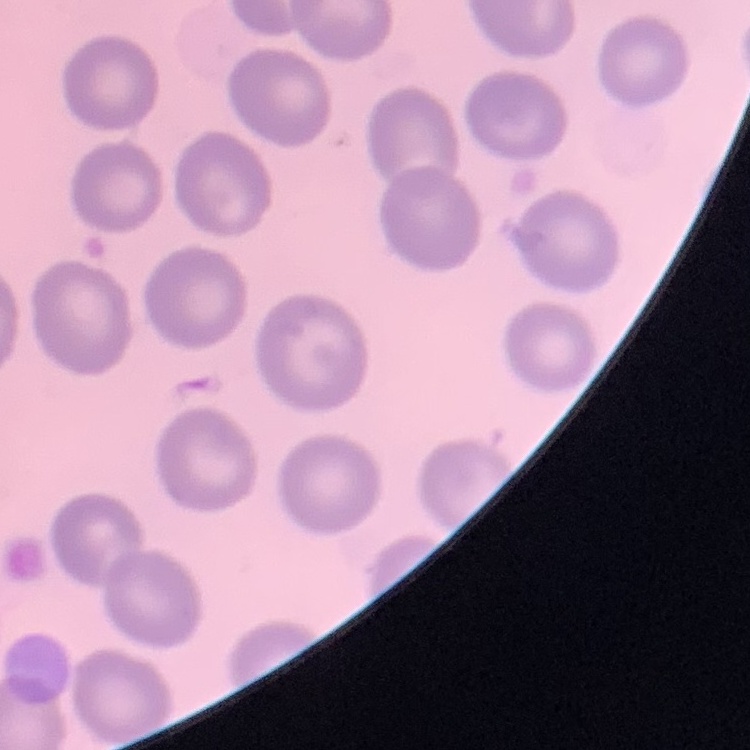

The erythrocytes exhibit no rouleaux formation. Stained with either Field's or Giemsa. One tile cut from a larger photomicrograph. Thin peripheral smear.